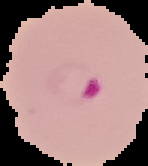

{
  "image_size": "148×166 pixels",
  "image_type": "segmented cell region with the area outside set to black",
  "result": "malaria parasites detected",
  "preparation": "thin blood smear"
}